Classify this cell by malaria status.
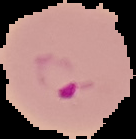

It is parasitized.

The area outside the segmented cell region is set to black. From a thin blood film. Image is 136×139 pixels.